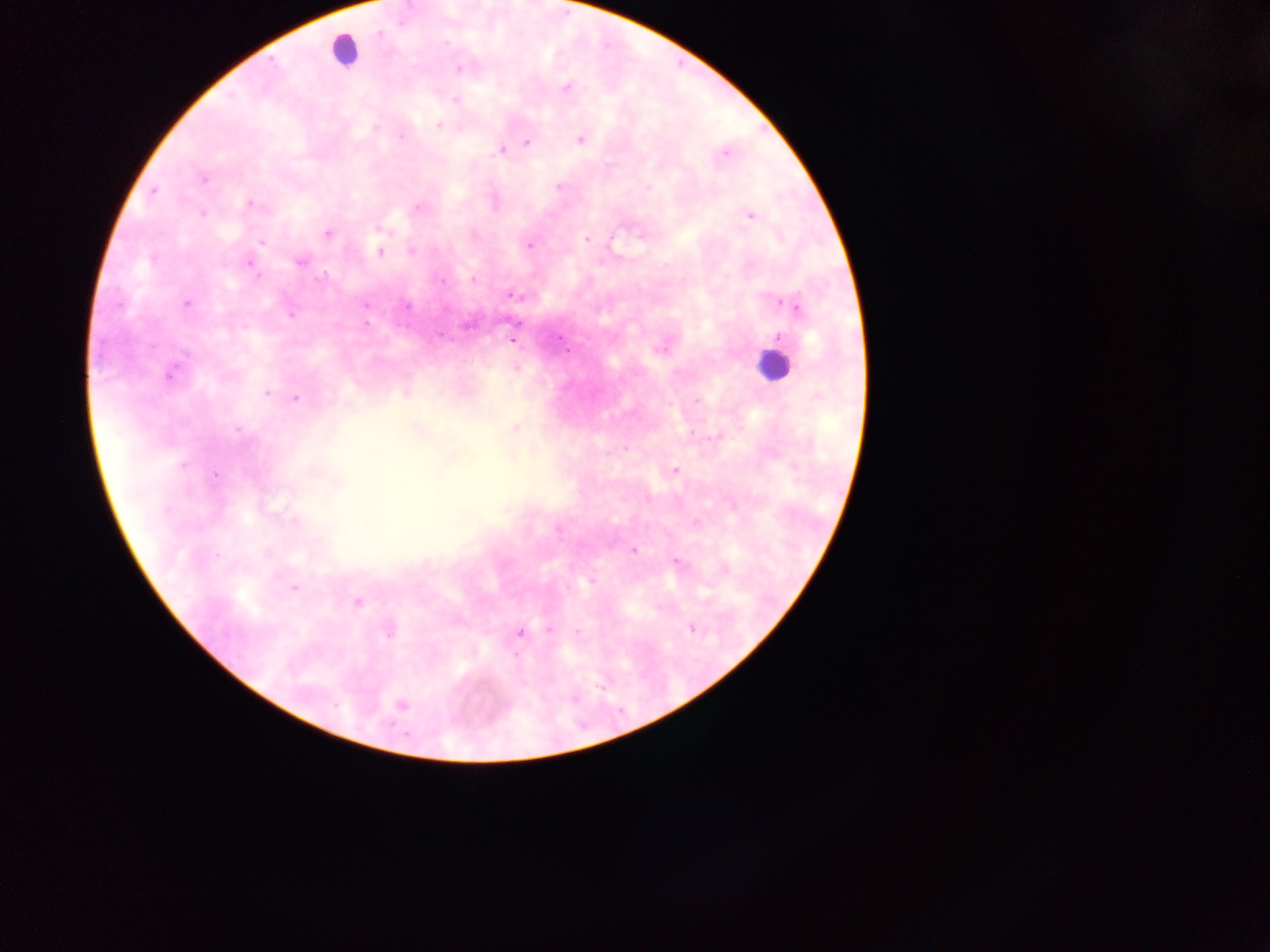

Approximate centers as (x, y) in pixels. Leukocyte locations: (344, 50), (774, 365). Plasmodium parasite locations: (458, 68), (566, 87), (455, 100), (438, 123), (581, 138), (527, 142), (502, 149), (725, 153), (202, 178), (559, 185), (153, 192), (494, 202), (250, 204), (419, 206), (201, 212), (750, 215), (328, 233), (586, 238), (528, 245), (380, 251), (299, 261), (248, 262), (472, 279), (513, 294), (186, 303), (365, 304), (512, 339), (661, 346), (517, 368), (170, 372), (266, 391), (406, 391), (295, 398), (515, 427), (418, 428), (674, 471), (733, 505), (696, 521), (633, 550), (677, 562), (724, 568), (590, 581), (356, 602), (388, 628), (692, 628), (550, 629), (519, 631), (577, 631), (400, 705). Image is 1270×952 pixels. Collected in Ghana. Single field of view. Photographed through a microscope with a mobile-phone camera. Thick blood film.